Name the blood parasite species.
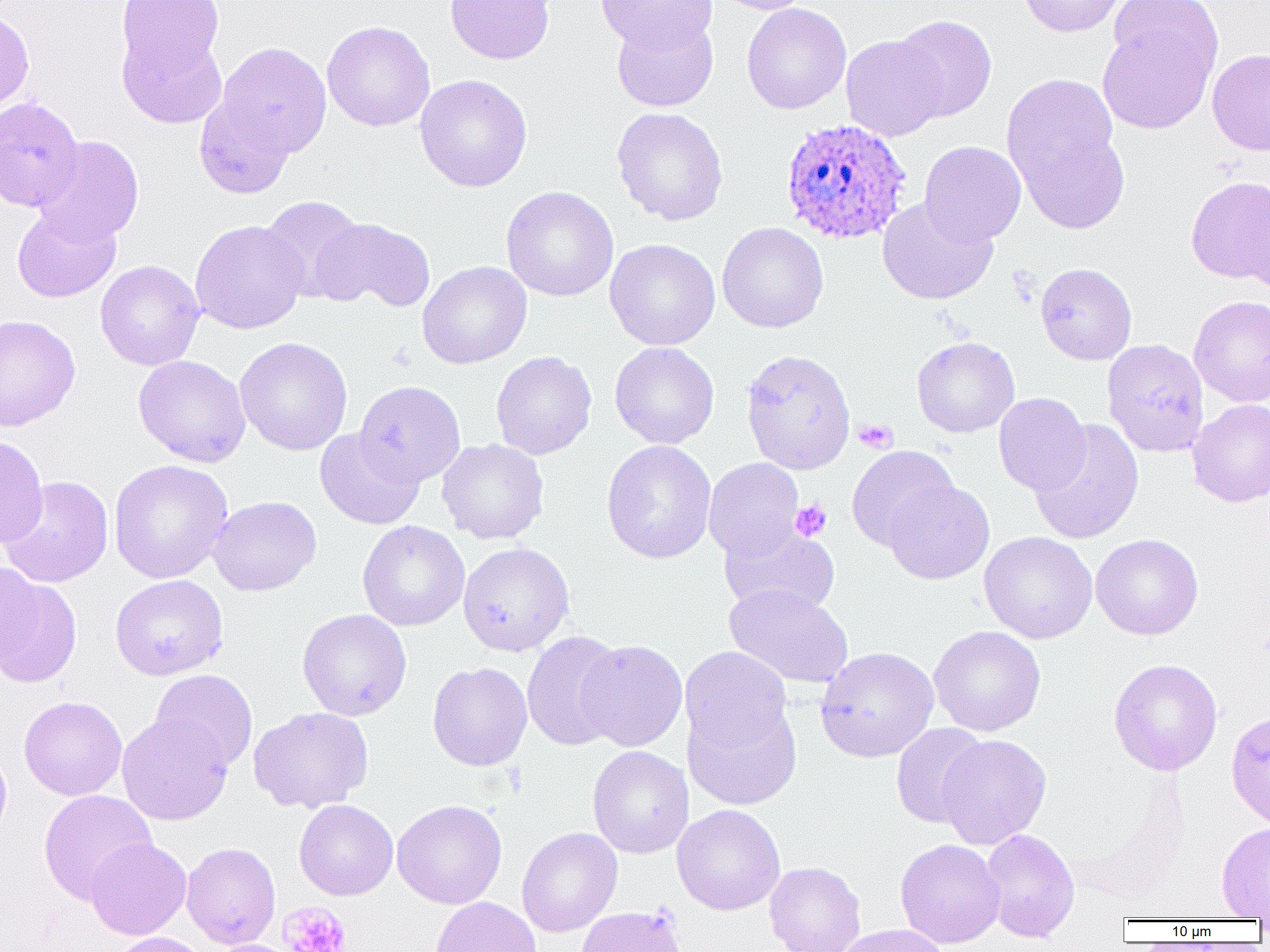

Plasmodium ovale.

Approximate bounding boxes as [x1, y1, x2, y2] in pixels. Plasmodium ovale-infected red blood cell locations: [780, 117, 912, 244]. Platelet locations: [853, 419, 897, 453], [790, 500, 832, 541], [279, 901, 352, 952]. Uninfected red blood cell locations: [115, 0, 227, 84], [445, 0, 555, 64], [596, 0, 716, 54], [714, 0, 814, 15], [1018, 0, 1126, 37], [1107, 0, 1221, 76], [741, 3, 851, 114], [0, 7, 34, 117], [612, 14, 718, 112], [892, 15, 997, 122], [1097, 17, 1219, 134], [322, 20, 435, 132], [117, 24, 229, 130], [841, 35, 947, 141], [215, 41, 332, 159], [1207, 48, 1270, 156], [1002, 73, 1122, 197], [414, 74, 532, 192], [194, 94, 296, 199], [0, 96, 84, 211], [611, 107, 729, 226], [1012, 123, 1130, 234], [33, 136, 144, 245], [919, 141, 1026, 245], [1185, 175, 1270, 286], [500, 186, 619, 301], [1240, 193, 1269, 297], [259, 195, 367, 301], [877, 197, 998, 305], [12, 204, 121, 303], [311, 217, 435, 313], [190, 220, 309, 334], [717, 222, 829, 333], [605, 238, 720, 351], [95, 260, 204, 371], [418, 261, 532, 369], [1035, 262, 1137, 365], [1188, 295, 1270, 408], [0, 314, 81, 431], [234, 336, 353, 456], [912, 336, 1019, 438], [1102, 338, 1209, 458], [609, 342, 719, 449], [740, 348, 856, 474], [491, 351, 597, 460], [133, 354, 251, 467], [354, 380, 466, 487], [994, 392, 1091, 496], [1187, 399, 1270, 507], [1029, 419, 1144, 544], [314, 428, 424, 530], [0, 434, 49, 548], [437, 439, 549, 544], [602, 439, 716, 564], [846, 445, 960, 551], [704, 458, 805, 561], [108, 459, 233, 584], [1, 476, 113, 587], [884, 480, 995, 584], [208, 495, 321, 596], [358, 520, 470, 631], [719, 523, 840, 618], [979, 531, 1097, 644], [1091, 534, 1203, 640], [458, 542, 574, 656], [0, 562, 43, 671], [1, 571, 83, 688], [109, 574, 228, 680], [724, 584, 854, 689], [297, 609, 412, 720], [928, 625, 1046, 736], [522, 630, 627, 751], [576, 639, 688, 751], [680, 646, 793, 752], [815, 646, 938, 762], [1108, 658, 1223, 775], [427, 662, 532, 771], [150, 669, 258, 771], [18, 695, 127, 801], [682, 698, 802, 811], [248, 707, 374, 813], [1226, 710, 1270, 829], [117, 713, 233, 825], [891, 722, 989, 828], [936, 734, 1052, 849], [0, 743, 12, 849], [587, 746, 693, 858], [38, 789, 157, 904], [294, 799, 398, 900], [392, 799, 507, 909], [672, 804, 785, 915], [1216, 822, 1270, 919], [516, 827, 622, 937], [980, 828, 1080, 943], [85, 837, 192, 940], [895, 838, 1005, 948], [181, 842, 280, 949], [765, 861, 866, 952], [431, 897, 541, 952], [575, 905, 687, 952], [834, 924, 949, 952], [109, 932, 211, 952], [205, 938, 303, 952]. Optical microscopy. Captured at 1000x magnification. Thin blood smear. Image is 1270×952 pixels. Single field of view.